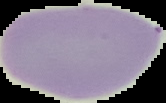
The area outside the segmented cell region is set to black. Result: no Plasmodium parasites seen. Image is 166×103 pixels. From a thin blood smear.